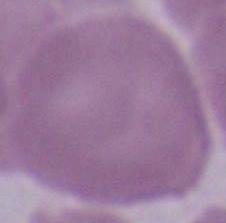

Summary:
  - Identification: red blood cell
  - Magnification: 1000x
  - Modality: photomicrograph